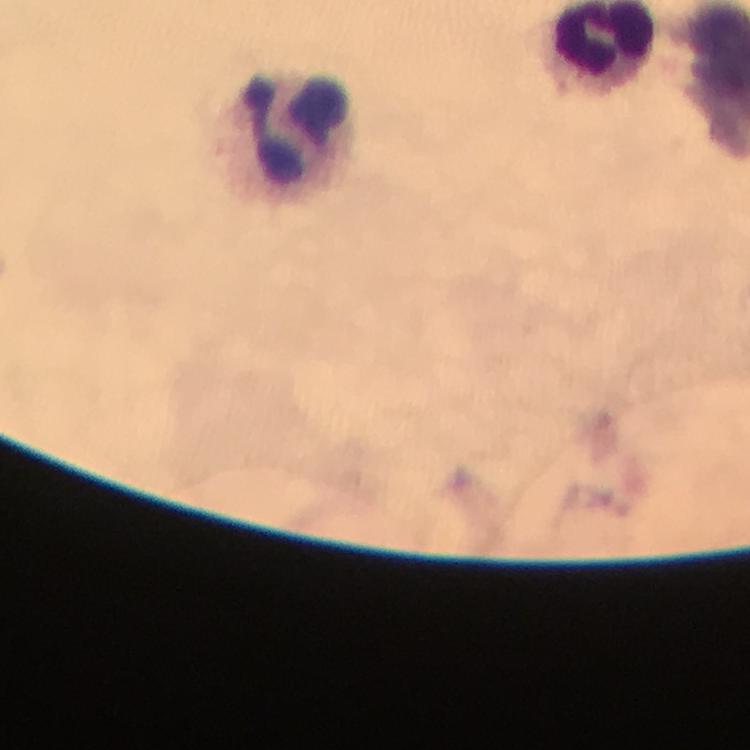
Approximate centers as {x, y} in pixels. Leukocyte locations: {297, 132}. Immersion oil was used. From a diagnostic examination for malaria. Cropped region of a single field of view. Giemsa-stained preparation. Image is 750×750 pixels. 100x magnification. Plasmodium parasites: none seen. Thick blood smear. Smartphone photograph taken through a microscope.